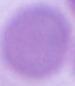
identification = erythrocyte
magnification = 1000x
modality = photomicrograph